Name the blood parasite species.
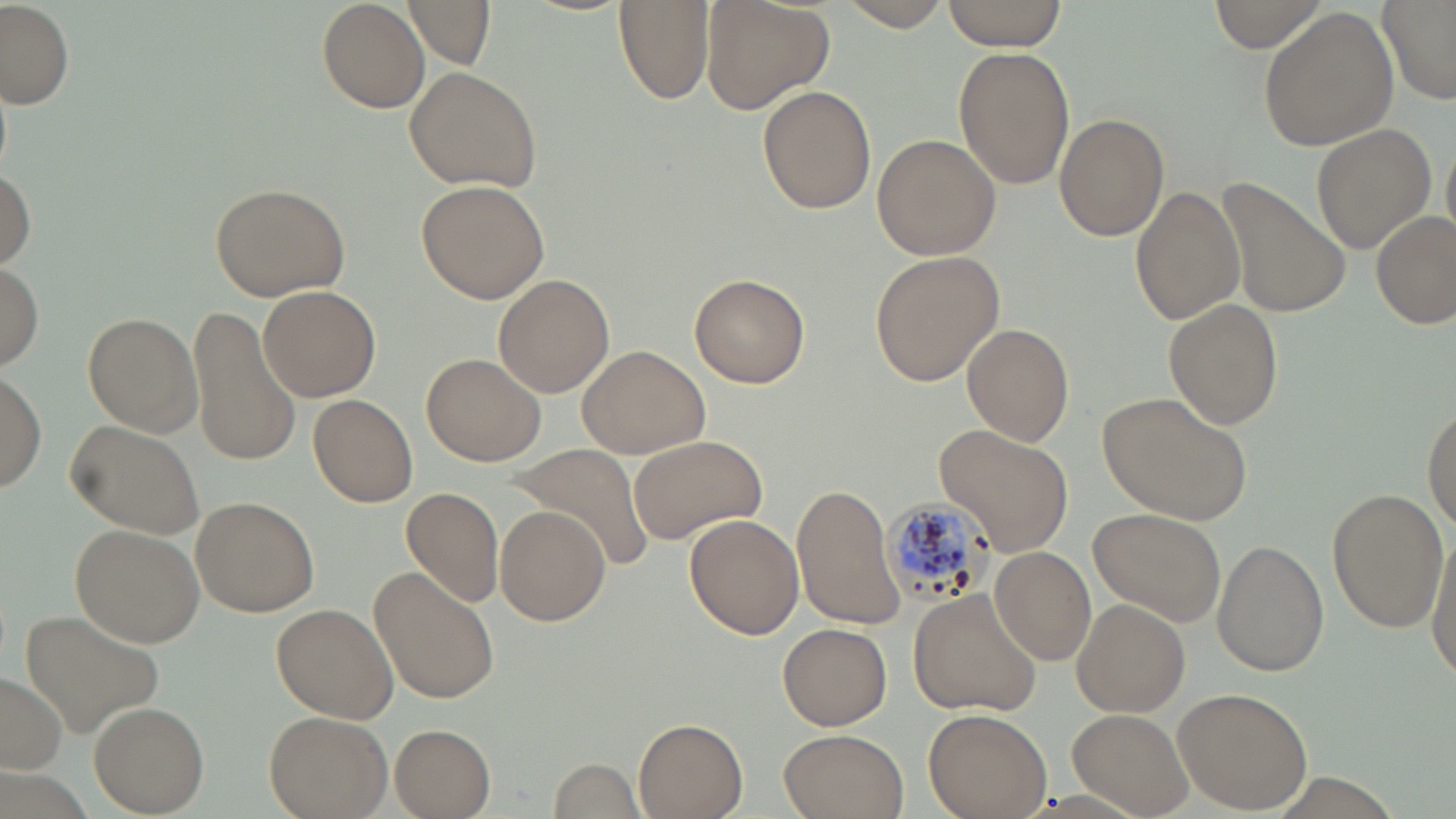

Plasmodium malariae.

Approximate bounding boxes as [x1, y1, x2, y2] in pixels. Uninfected red blood cell locations: [318, 0, 428, 112], [403, 0, 496, 67], [836, 0, 955, 33], [941, 0, 1066, 51], [1208, 0, 1329, 52], [1377, 0, 1455, 105], [614, 1, 713, 106], [701, 1, 834, 114], [2, 2, 74, 110], [1258, 8, 1399, 152], [954, 48, 1075, 191], [404, 66, 543, 191], [756, 85, 876, 214], [1055, 113, 1169, 242], [1314, 125, 1435, 251], [872, 134, 1000, 261], [0, 166, 35, 268], [418, 178, 551, 304], [1219, 178, 1351, 318], [209, 181, 352, 300], [1130, 185, 1246, 325], [1370, 211, 1454, 330], [871, 248, 1006, 387], [0, 260, 44, 374], [690, 273, 811, 388], [492, 274, 614, 398], [258, 285, 381, 402], [206, 290, 358, 435], [1164, 298, 1284, 430], [187, 306, 303, 469], [81, 312, 205, 437], [962, 323, 1075, 446], [578, 345, 710, 459], [421, 351, 547, 467], [0, 369, 47, 492], [1098, 392, 1253, 522], [307, 396, 420, 509], [1423, 401, 1456, 531], [63, 418, 205, 541], [932, 425, 1076, 559], [628, 432, 770, 547], [511, 443, 655, 573], [791, 481, 907, 630], [401, 486, 504, 609], [1330, 486, 1449, 633], [191, 496, 321, 617], [494, 506, 610, 625], [1089, 507, 1226, 628], [684, 513, 805, 640], [70, 523, 204, 647], [1427, 525, 1456, 687], [1213, 539, 1329, 676], [989, 547, 1097, 664], [370, 568, 498, 704], [908, 589, 1042, 718], [1069, 600, 1190, 717], [270, 603, 399, 724], [22, 610, 165, 737], [778, 621, 893, 730], [0, 672, 68, 774], [1171, 687, 1314, 813], [89, 702, 208, 815], [1067, 707, 1194, 817], [261, 708, 391, 819], [924, 708, 1051, 818], [634, 718, 749, 818], [389, 724, 496, 817], [776, 729, 912, 819], [548, 760, 647, 815]. Plasmodium malariae-infected red blood cell locations: [888, 494, 994, 608]. Image is 1456×819 pixels. One field of a larger specimen. May-Grünwald-Giemsa-stained preparation. 1000x magnification. Optical microscopy. Thin blood smear.